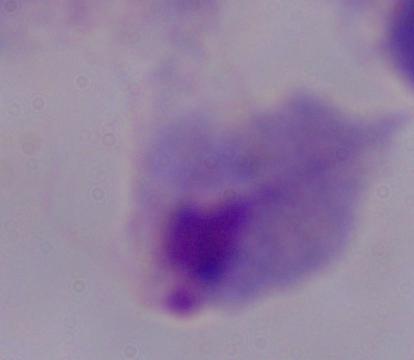

identification: trichomonad
magnification: 1000x
modality: micrograph